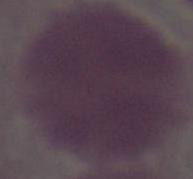
Summary:
  - Identification: erythrocyte
  - Modality: photomicrograph
  - Magnification: 1000x